Assess this cell for malaria.
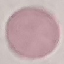
Uninfected.

Summary:
  - Capture: smartphone camera at the microscope eyepiece
  - Image type: automatically extracted cell patch, resized to 64 × 64 pixels
  - Preparation: thin smear
  - Stain: Giemsa